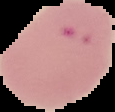 Segmented cell region on a black background. Malaria status: parasitized. From a thin blood film. Image is 115×112 pixels.